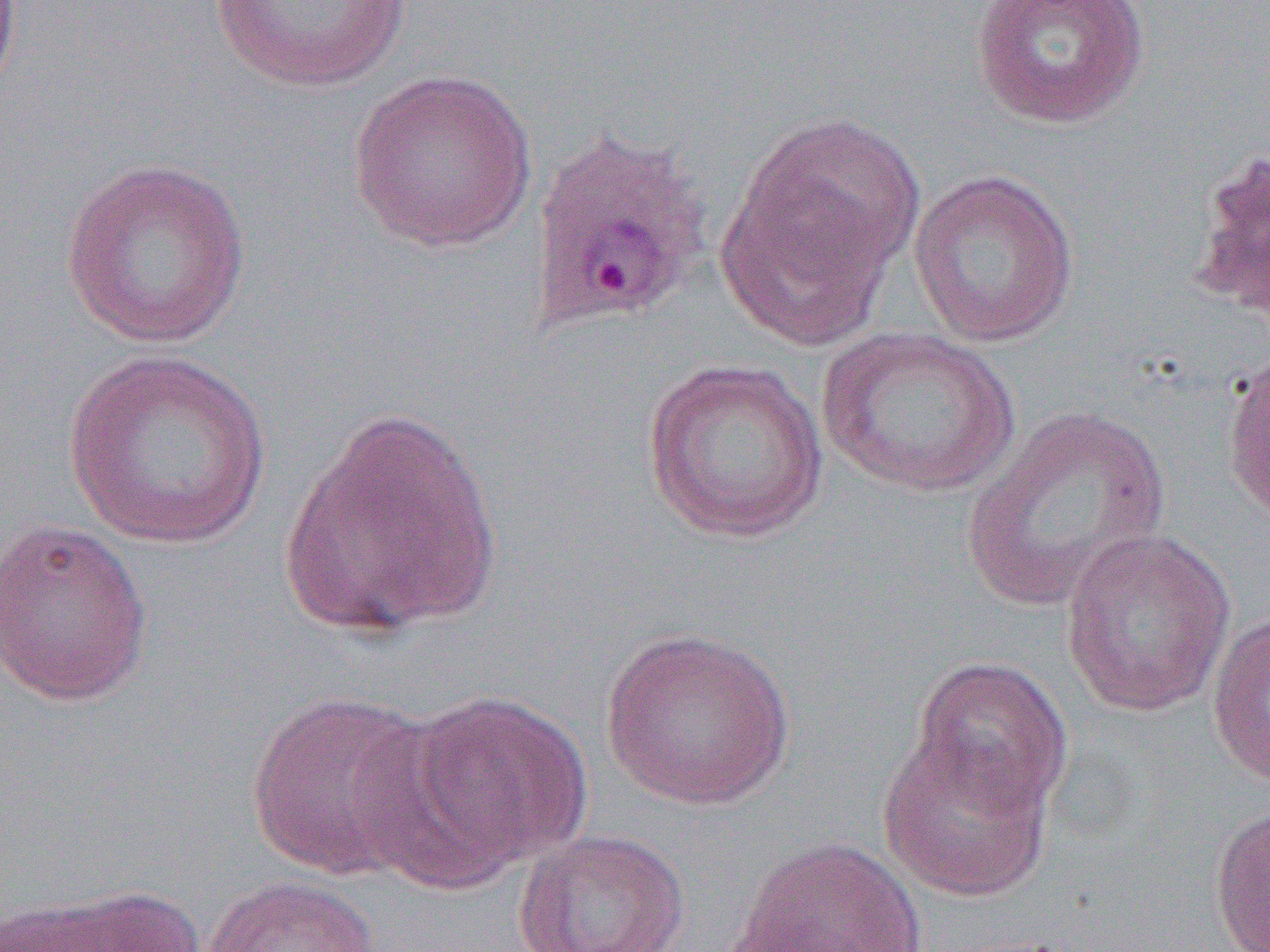

slide-level diagnosis = Plasmodium ovale
magnification = 1000x
image size = 1270×952 pixels
field of view = one of a larger specimen
modality = optical microscopy
uninfected red blood cell locations = approximate bounding boxes as named x1/y1/x2/y2 corners in pixels: (x1=204, y1=0, x2=420, y2=92), (x1=970, y1=0, x2=1152, y2=129), (x1=346, y1=68, x2=539, y2=255), (x1=722, y1=116, x2=926, y2=333), (x1=1187, y1=145, x2=1270, y2=330), (x1=59, y1=156, x2=253, y2=351), (x1=908, y1=169, x2=1080, y2=349), (x1=816, y1=326, x2=1020, y2=499), (x1=61, y1=349, x2=274, y2=550), (x1=1222, y1=350, x2=1270, y2=526), (x1=640, y1=358, x2=829, y2=544), (x1=961, y1=404, x2=1172, y2=611), (x1=280, y1=405, x2=503, y2=639), (x1=0, y1=518, x2=153, y2=707), (x1=1060, y1=528, x2=1236, y2=718), (x1=1205, y1=606, x2=1270, y2=787), (x1=599, y1=627, x2=797, y2=811), (x1=908, y1=655, x2=1074, y2=820), (x1=401, y1=688, x2=594, y2=877), (x1=245, y1=689, x2=442, y2=884), (x1=877, y1=732, x2=1057, y2=903), (x1=1208, y1=803, x2=1269, y2=952), (x1=514, y1=828, x2=690, y2=952), (x1=729, y1=836, x2=929, y2=952), (x1=200, y1=875, x2=381, y2=952), (x1=10, y1=884, x2=208, y2=952)
Plasmodium ovale-infected red blood cell locations = approximate bounding boxes as named x1/y1/x2/y2 corners in pixels: (x1=526, y1=125, x2=714, y2=337)
preparation = thin blood smear